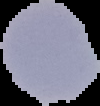

Image is 100×106 pixels. Malaria status: parasitized. From a thin blood smear. Cell region segmented out of the field of view; the surrounding area is masked to black.